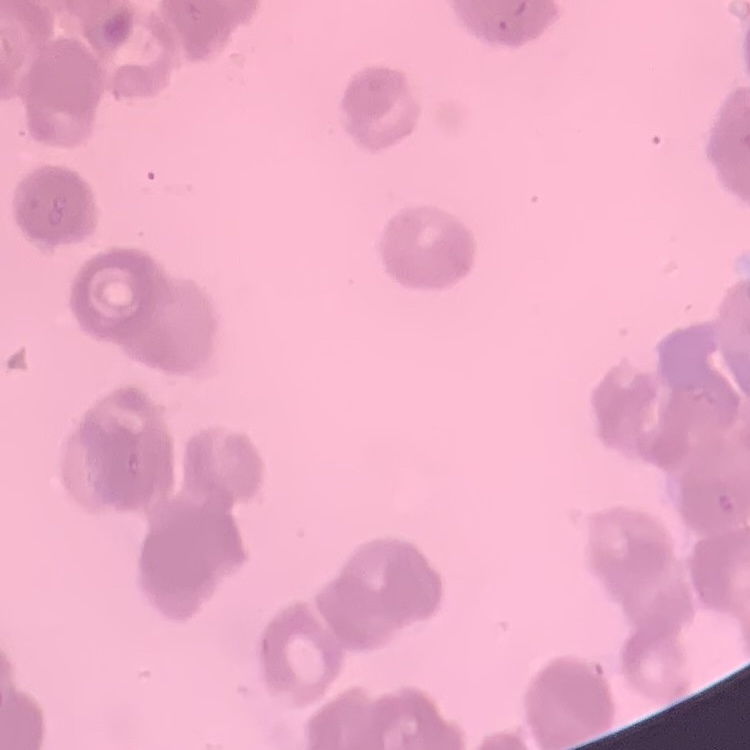 The red blood cells show rouleaux formation. Square crop of a larger photomicrograph. Stained with either Field's or Giemsa. Thin blood film.